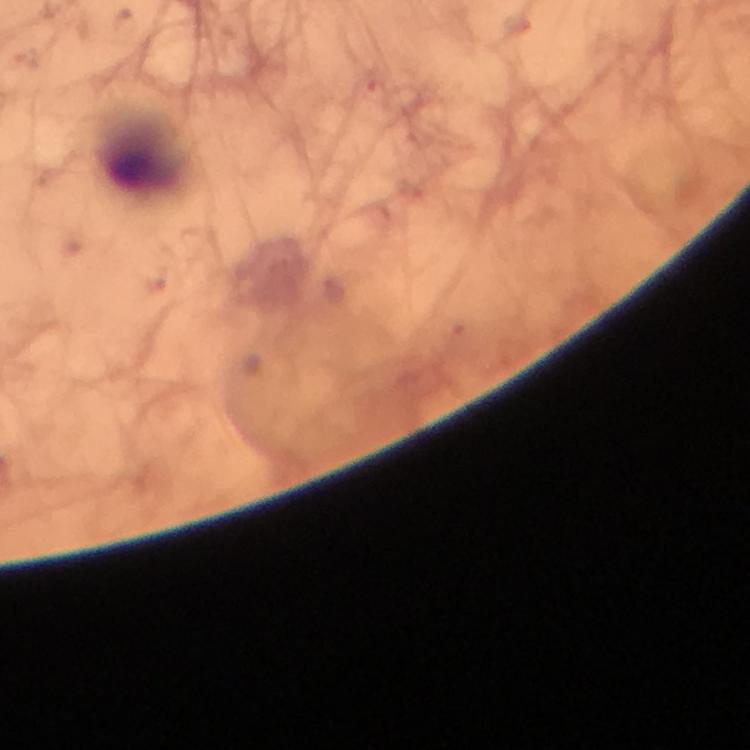

Approximate centers as (x, y) in pixels.
Summary:
  - Leukocyte locations: (145, 148)
  - Cropped from: a single field of view
  - Magnification: 100x
  - Immersion oil: applied
  - Malaria parasites: none seen
  - Capture: smartphone mounted on the microscope
  - Stain: Giemsa
  - Context: from a malaria diagnostic workup
  - Image size: 750×750 pixels
  - Preparation: thick blood smear